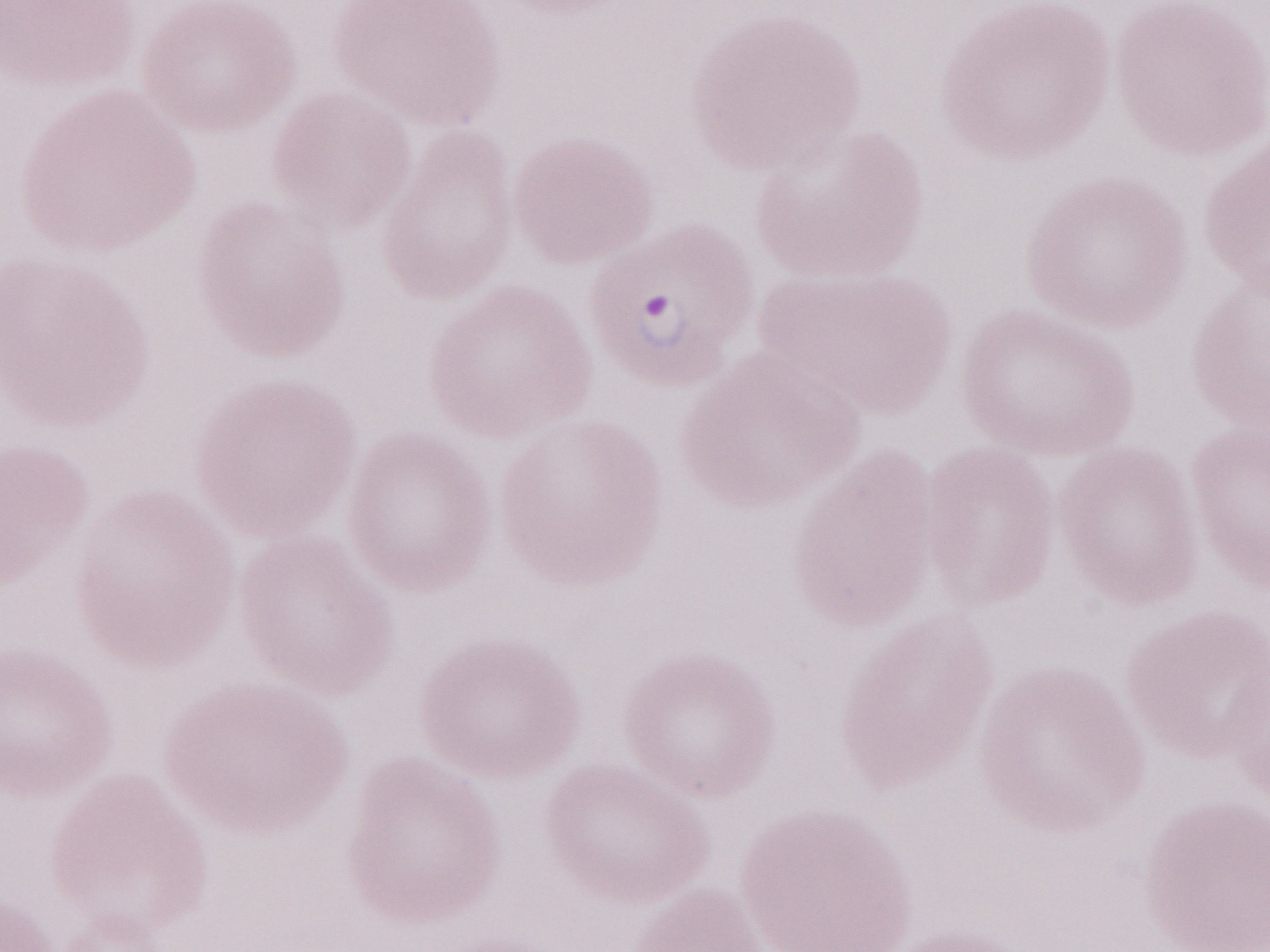

Malaria diagnosis (patient-level): positive. Magnification: 1,000x. Image is 1270×952 pixels. May-Grünwald-Giemsa (MGG) stain. Olympus BX43 microscope and DP73 digital camera. Thin blood smear. One field of this slide.